Report the malaria status of this cell.
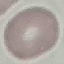

Uninfected.

Acquired by smartphone through the microscope eyepiece. Automatically extracted cell patch, resized to 64 × 64 pixels. Giemsa-stained preparation. Thin blood smear.